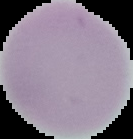
Summary:
  - Image type: segmented cell region with the area outside set to black
  - Malaria status: uninfected
  - Preparation: thin blood film
  - Image size: 133×139 pixels